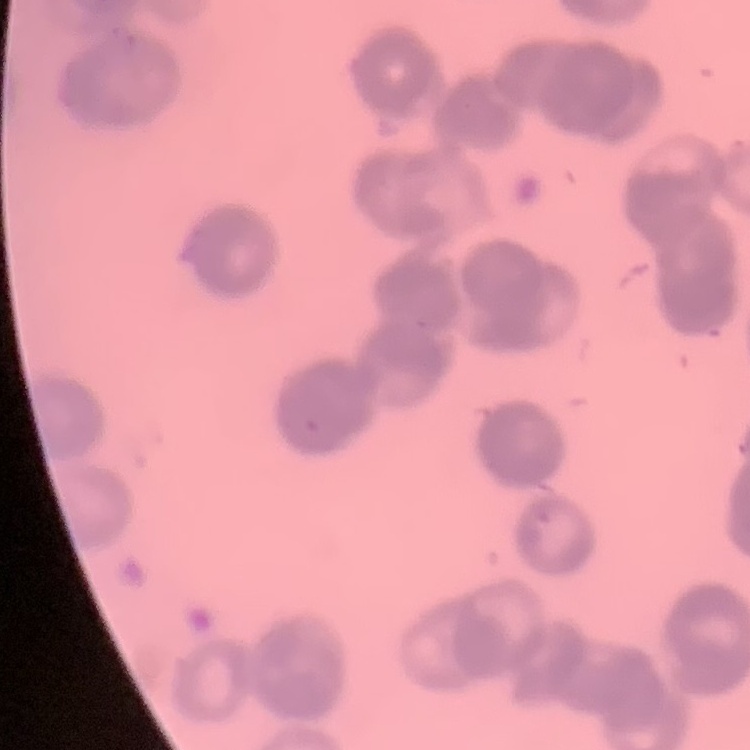

erythrocyte morphology = rouleaux formation
image type = square crop of a larger photomicrograph
preparation = thin blood film
stain = Field's or Giemsa